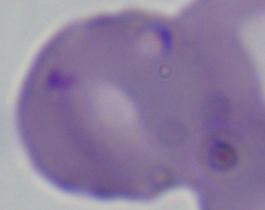

Summary:
  - Modality: micrograph
  - Magnification: 1000x
  - Identification: Babesia